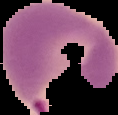
image size = 118×115 pixels
image type = cell region segmented out of the field of view; surrounding area masked to black
result = malaria parasites detected
preparation = thin blood smear